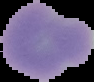
{
  "image_size": "94×82 pixels",
  "image_type": "cell region segmented out of the field of view; surrounding area masked to black",
  "result": "negative for malaria parasites",
  "preparation": "thin blood smear"
}